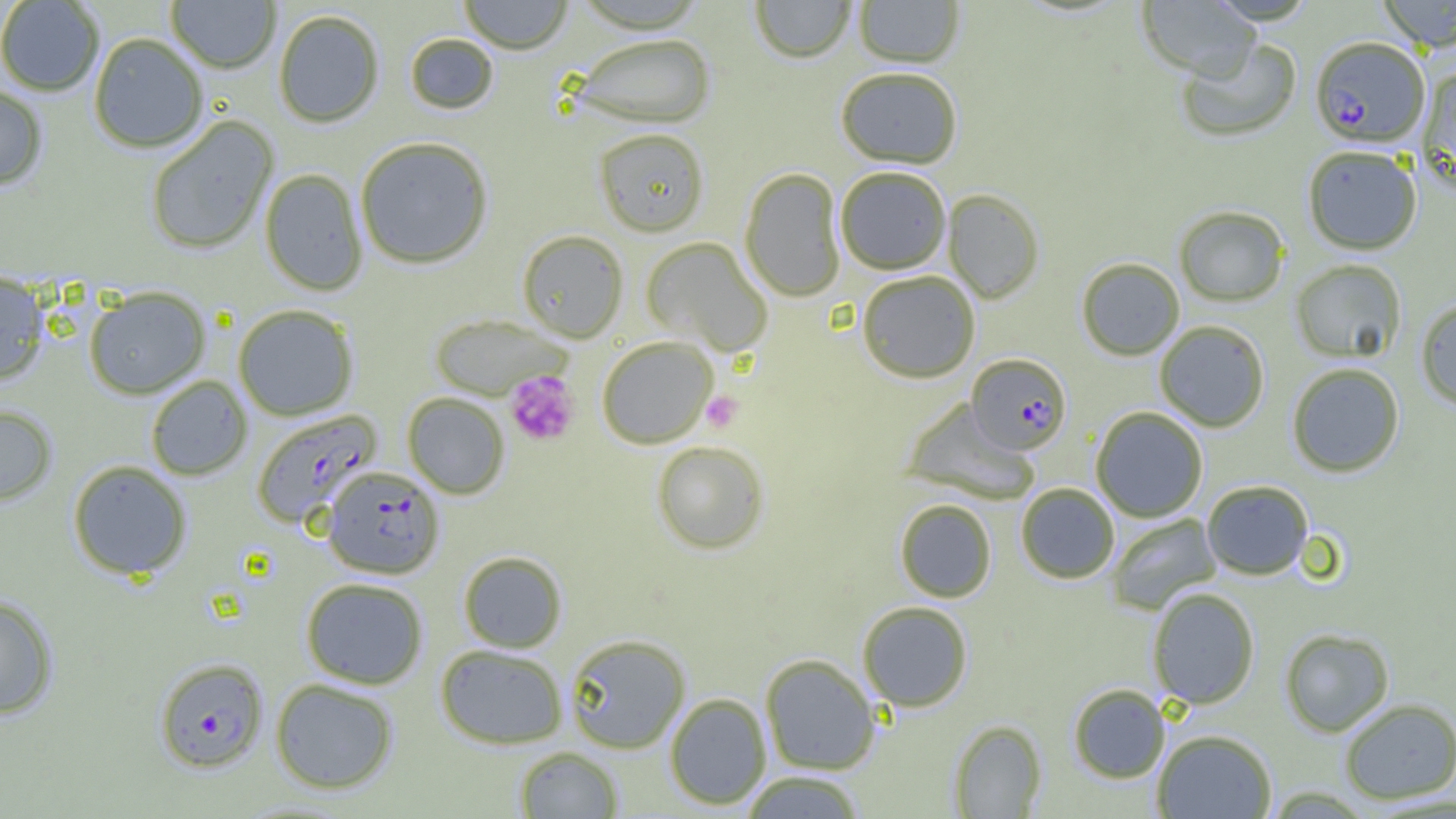
Summary:
  - Coordinate format: approximate bounding boxes as [x1, y1, x2, y2] in pixels
  - Platelet locations: [505, 371, 579, 446], [701, 391, 743, 433]
  - Uninfected red blood cell locations: [166, 0, 281, 74], [458, 0, 573, 54], [750, 0, 856, 64], [853, 0, 964, 68], [1136, 0, 1260, 81], [1377, 0, 1456, 51], [0, 1, 104, 97], [274, 9, 385, 128], [88, 33, 209, 153], [405, 33, 499, 115], [572, 34, 715, 129], [1176, 37, 1301, 143], [835, 67, 963, 169], [1416, 67, 1456, 196], [0, 83, 49, 191], [145, 116, 279, 255], [594, 129, 709, 237], [354, 136, 494, 269], [1303, 146, 1422, 255], [835, 166, 951, 275], [259, 168, 368, 296], [739, 168, 846, 302], [943, 189, 1044, 303], [1174, 205, 1290, 306], [517, 230, 628, 342], [641, 237, 773, 357], [1076, 257, 1185, 361], [1290, 259, 1407, 363], [857, 270, 980, 383], [0, 272, 50, 385], [84, 286, 210, 399], [1415, 299, 1456, 409], [233, 305, 359, 421], [430, 315, 571, 400], [1154, 320, 1270, 432], [596, 336, 718, 449], [1286, 362, 1405, 477], [145, 375, 252, 481], [402, 393, 510, 499], [901, 400, 1040, 505], [0, 404, 58, 506], [1091, 407, 1208, 522], [651, 441, 769, 555], [67, 460, 193, 580], [1201, 480, 1314, 580], [1016, 482, 1120, 583], [894, 499, 996, 603], [1107, 513, 1221, 615], [458, 550, 568, 653], [301, 577, 428, 689], [1147, 587, 1260, 709], [0, 594, 59, 719], [857, 601, 973, 712], [1279, 628, 1394, 737], [565, 634, 691, 754], [435, 644, 568, 749], [760, 654, 881, 775], [270, 678, 399, 794], [1068, 683, 1169, 783], [664, 692, 772, 810], [1339, 698, 1456, 804], [949, 719, 1047, 817], [1152, 729, 1277, 818], [514, 747, 623, 818], [739, 771, 868, 818]
  - Plasmodium falciparum-infected red blood cell locations: [1310, 36, 1429, 147], [966, 353, 1072, 455], [251, 409, 382, 528], [321, 466, 444, 579], [154, 657, 268, 772]
  - Slide-level diagnosis: Plasmodium falciparum
  - Magnification: 1000x
  - Modality: light microscopy
  - Field of view: single
  - Preparation: thin blood film
  - Image size: 1456×819 pixels